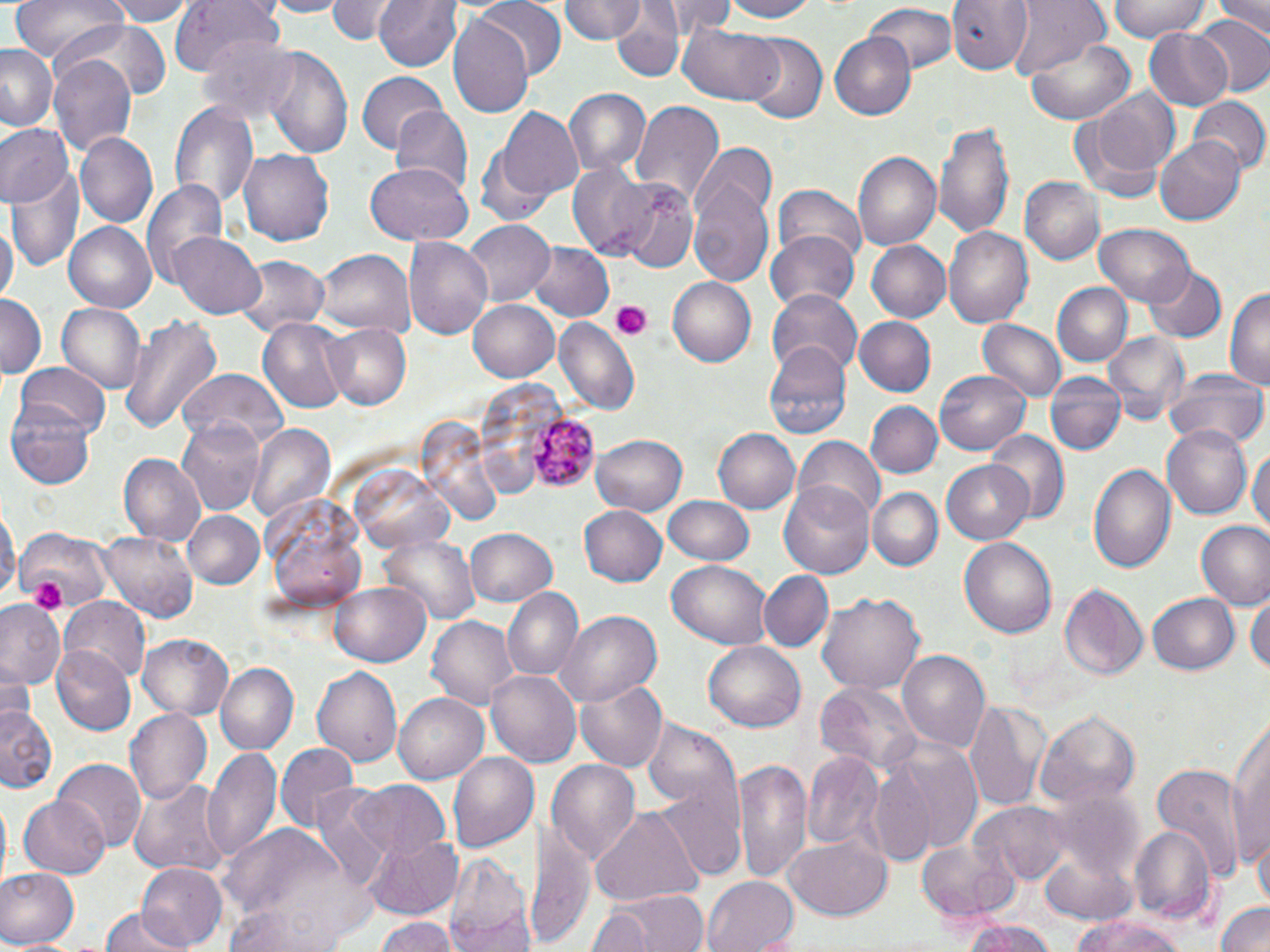
Summary:
  - Coordinate format: approximate bounding boxes as (x1,y1)-(x2,y2) corner pairs in pixels
  - Platelet locations: (608,300)-(655,341), (29,574)-(69,613)
  - Plasmodium malariae-infected red blood cell locations: (527,413)-(603,491)
  - Uninfected red blood cell locations: (10,0)-(126,66), (110,0)-(194,26), (167,0)-(284,78), (260,0)-(349,18), (327,0)-(397,43), (375,0)-(463,72), (477,0)-(564,79), (558,0)-(646,43), (658,0)-(730,38), (718,0)-(823,23), (946,0)-(1034,74), (1105,0)-(1213,42), (1215,0)-(1269,38), (1007,1)-(1109,78), (863,4)-(958,79), (609,8)-(684,83), (1192,15)-(1270,97), (448,16)-(533,118), (62,23)-(166,111), (682,23)-(786,106), (1142,27)-(1236,111), (199,31)-(301,128), (830,32)-(916,119), (741,35)-(826,124), (1027,39)-(1137,125), (0,46)-(60,132), (264,47)-(354,161), (49,57)-(135,155), (356,70)-(447,153), (1074,89)-(1179,197), (564,90)-(651,175), (1189,97)-(1269,176), (169,101)-(259,212), (630,101)-(724,204), (392,107)-(474,201), (496,108)-(584,202), (933,119)-(1016,239), (0,125)-(74,210), (75,133)-(157,230), (1155,137)-(1245,225), (696,144)-(777,224), (238,146)-(337,246), (852,151)-(941,251), (9,158)-(84,278), (566,161)-(659,260), (364,162)-(472,247), (689,168)-(775,286), (1015,175)-(1101,263), (142,179)-(228,292), (770,185)-(867,272), (620,186)-(699,273), (0,217)-(16,312), (461,219)-(555,308), (65,221)-(156,312), (1094,225)-(1196,308), (944,228)-(1034,328), (170,231)-(266,318), (768,231)-(861,315), (405,235)-(493,338), (867,240)-(951,323), (523,242)-(614,324), (314,249)-(414,338), (234,256)-(329,337), (1143,264)-(1226,342), (668,278)-(756,368), (1051,282)-(1132,369), (1226,286)-(1269,392), (769,288)-(863,377), (0,293)-(45,376), (467,298)-(561,382), (56,301)-(147,394), (119,313)-(221,435), (551,315)-(639,414), (853,316)-(937,397), (258,319)-(349,410), (978,320)-(1067,403), (324,323)-(411,410), (1105,332)-(1192,424), (764,342)-(851,443), (12,363)-(110,445), (1166,367)-(1267,450), (934,370)-(1031,457), (180,371)-(287,451), (1044,372)-(1128,457), (476,380)-(566,500), (865,401)-(941,479), (6,402)-(97,489), (175,417)-(266,516), (410,419)-(509,524), (1163,422)-(1255,519), (248,424)-(335,526), (712,427)-(799,514), (989,429)-(1068,524), (592,433)-(688,515), (791,436)-(885,525), (1250,443)-(1269,539), (118,455)-(206,545), (940,458)-(1036,544), (1088,460)-(1177,576), (353,464)-(458,554), (780,479)-(875,577), (867,486)-(944,574), (259,491)-(369,614), (663,495)-(755,565), (1,500)-(17,606), (580,504)-(669,587), (183,511)-(265,589), (1195,520)-(1270,610), (465,525)-(559,608), (12,529)-(113,613), (99,531)-(198,623), (381,533)-(479,627), (958,533)-(1057,635), (669,560)-(770,649), (760,571)-(832,651), (329,583)-(432,667), (1058,584)-(1148,683), (1248,584)-(1268,685), (500,587)-(585,680), (1148,590)-(1239,676), (817,591)-(924,697), (59,599)-(150,685), (0,601)-(66,688), (559,611)-(659,706), (426,616)-(519,709), (137,634)-(235,721), (703,639)-(804,730), (50,645)-(136,735), (896,648)-(991,753), (214,662)-(298,754), (310,663)-(402,765), (0,665)-(34,726), (485,669)-(580,766), (576,678)-(666,774), (815,682)-(920,776), (392,693)-(489,783), (967,698)-(1050,812), (1,703)-(59,794), (124,708)-(212,805), (1036,709)-(1141,809), (1230,712)-(1270,868), (878,740)-(986,862), (276,742)-(355,831), (206,748)-(282,864), (449,751)-(539,853), (802,754)-(886,853), (733,756)-(812,887), (545,757)-(640,861), (53,760)-(146,853), (1151,764)-(1248,884), (128,779)-(227,875), (352,780)-(451,861), (1042,788)-(1141,887), (19,795)-(111,878), (976,799)-(1069,884), (591,806)-(702,908), (528,817)-(593,952), (219,824)-(360,949), (1128,824)-(1214,923), (360,830)-(463,916), (1251,833)-(1270,914), (785,834)-(893,920), (916,840)-(1022,924), (447,850)-(529,949), (1041,855)-(1136,925), (137,862)-(226,948), (0,868)-(77,950), (703,874)-(799,951), (591,888)-(711,952), (1216,899)-(1270,952), (585,904)-(656,952), (226,906)-(346,952), (98,908)-(189,952), (1072,914)-(1186,952), (374,917)-(457,952), (960,924)-(1059,952)
  - Slide-level diagnosis: Plasmodium malariae
  - Field of view: one of a larger specimen
  - Stain: May-Grünwald-Giemsa
  - Modality: light microscopy
  - Image size: 1270×952 pixels
  - Magnification: 1000x
  - Preparation: thin blood film